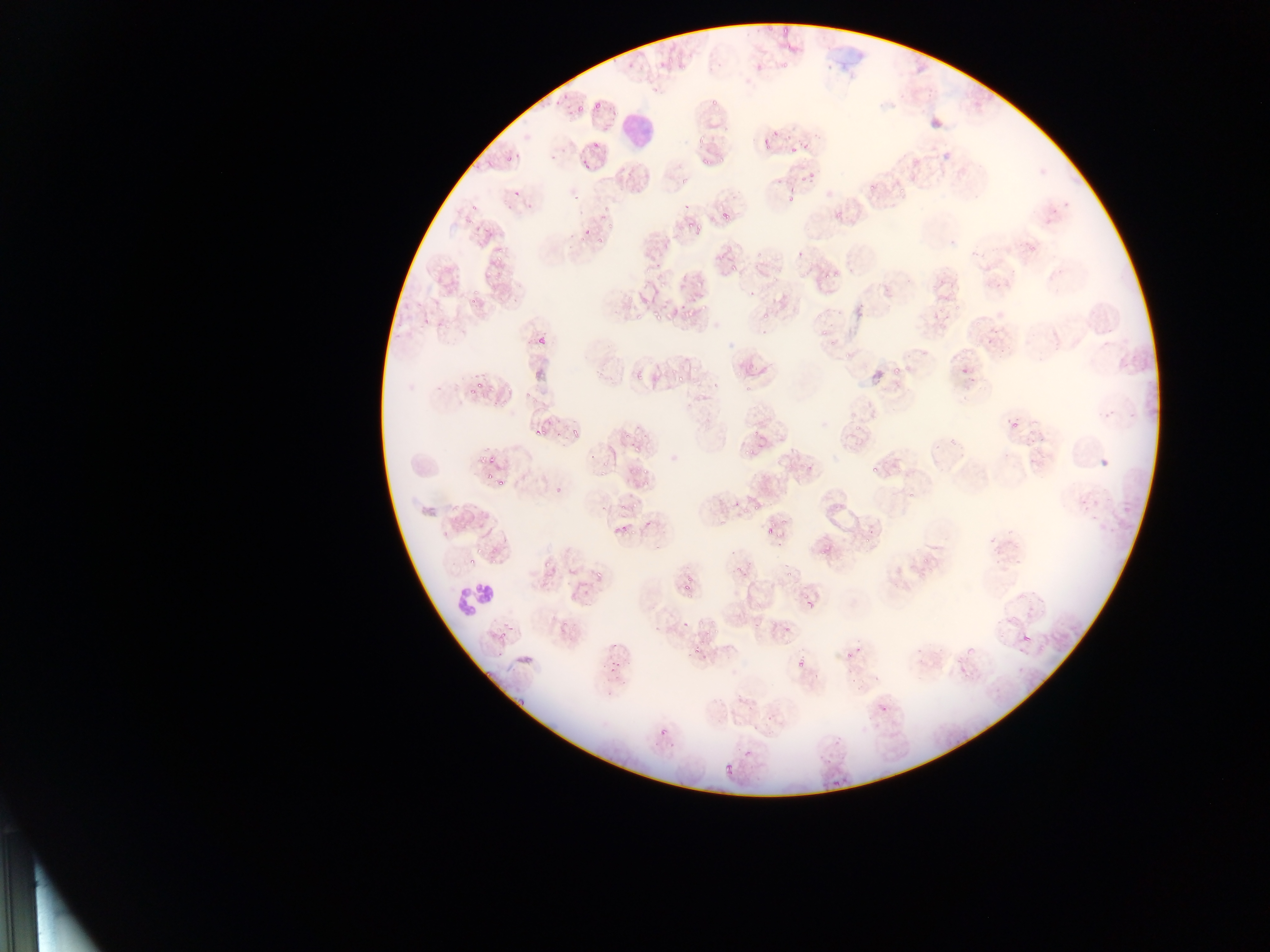 Approximate bounding boxes as left top right bottom in pixels. Plasmodium parasite locations: 782 26 791 36; 766 29 776 41; 782 56 791 71; 574 93 588 116; 590 97 609 123; 707 97 717 109; 694 136 706 148; 763 140 773 153; 580 147 594 170; 791 147 797 157; 504 152 514 163; 719 153 724 174; 699 159 707 169; 808 170 815 181; 868 184 875 194; 901 188 907 200; 463 190 486 217; 786 190 799 207; 595 205 608 220; 722 213 732 223; 833 214 840 225; 607 216 621 228; 693 223 705 234; 577 227 594 241; 597 234 605 243; 494 242 505 253; 725 261 742 275; 826 263 839 281; 467 276 486 308; 680 298 700 318; 650 311 659 318; 814 322 832 337; 537 335 548 348; 694 359 704 375; 632 364 647 384; 954 366 967 381; 891 367 900 376; 675 375 682 383; 478 382 487 393; 464 386 474 396; 491 401 502 412; 854 415 864 437; 1008 419 1019 432; 570 423 582 436; 534 424 541 434; 536 428 554 435; 621 431 627 440; 742 440 756 460; 630 443 642 454; 477 453 489 464; 1096 454 1114 473; 868 462 877 471; 805 463 815 475; 598 465 607 476; 626 465 636 473; 641 468 653 479; 482 475 490 482; 496 478 507 489; 553 481 567 493; 751 497 762 513; 632 499 640 512; 763 515 784 533; 619 523 628 537; 861 533 874 547; 630 535 641 539; 772 538 779 546; 818 544 832 558; 542 555 554 573; 461 556 478 568; 921 558 928 567; 595 563 609 577; 784 570 793 577; 679 579 691 596; 806 593 817 610; 784 621 793 633; 699 624 716 646; 1018 630 1034 649; 496 632 507 639; 691 645 705 655; 608 649 629 674; 842 652 852 664; 795 657 808 671; 874 699 896 722; 659 727 670 739; 822 754 836 772; 722 761 735 774 | approximate x y pixel centers of objects too small to bound: 802 177; 518 190; 604 509; 621 509. Leukocyte locations: 620 103 661 157; 454 574 503 618. Photographed through a microscope with a mobile-phone camera. Single field of view. Sample from Ghana. Thin blood film. Image is 1270×952 pixels.